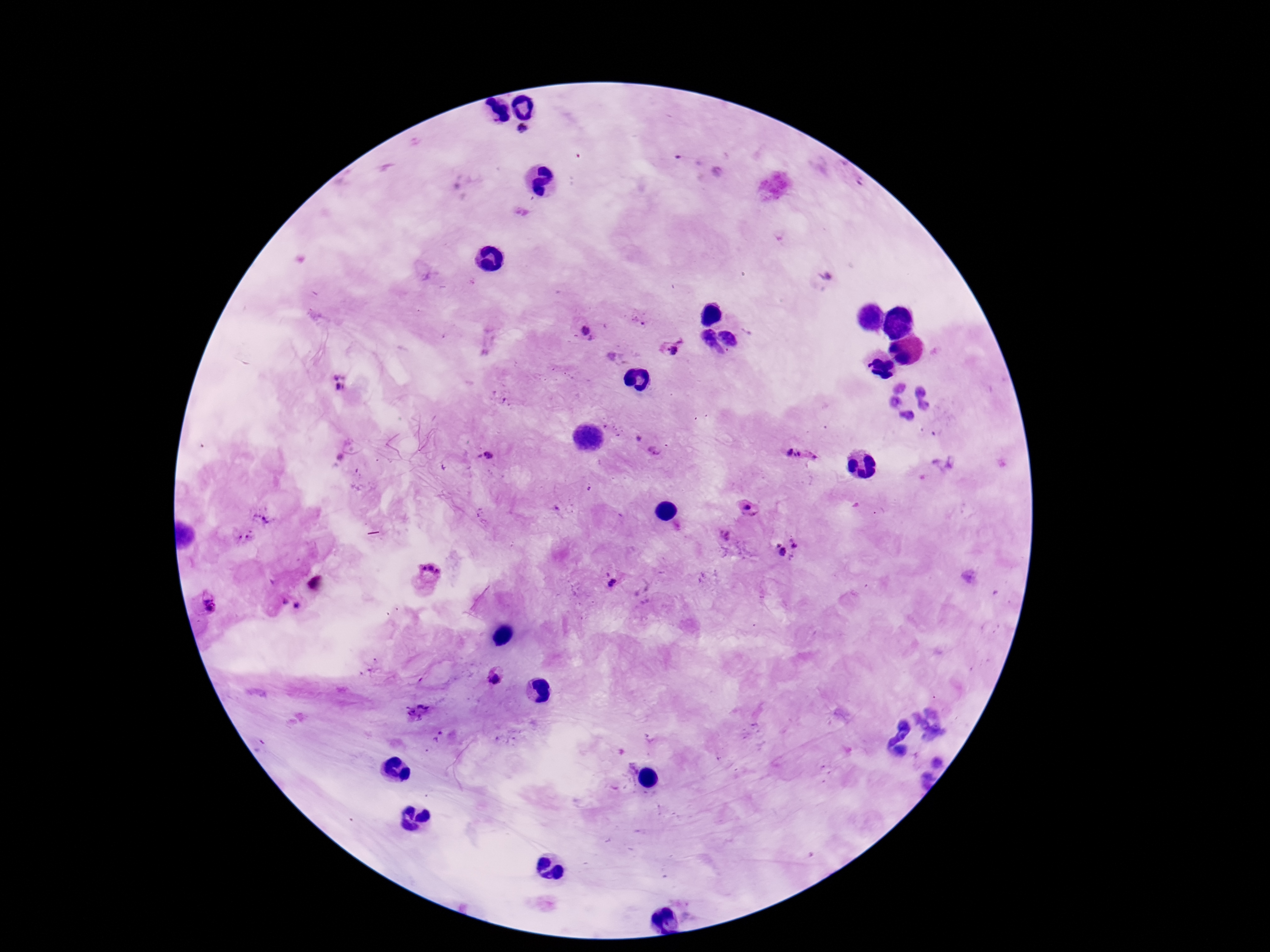

field_of_view: one from this slide
patient_malaria_status: positive
stain: Giemsa
plasmodium_parasite_locations: 'approximate centers as {x, y} in pixels: {523, 133}, {585, 332}, {670, 346}, {618, 359}, {339, 383}, {636, 440}, {655, 452}, {487, 456}, {803, 456}, {748, 507}, {263, 516}, {244, 539}, {788, 548}, {428, 574}, {611, 583}, {207, 604}, {496, 674}, {417, 713}'
preparation: thick blood smear
capture: smartphone camera through the microscope eyepiece
magnification: 100x
image_size: 1270×952 pixels